Name the cell type shown.
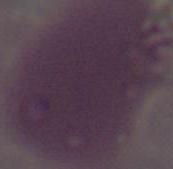
An erythrocyte.

Micrograph. 1000x magnification.